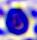 Captured at 400x magnification. A leukocyte is shown. Micrograph.